Classify this cell by malaria status.
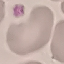
Uninfected.

Thin smear of blood. Giemsa-stained preparation. Acquired by smartphone through the microscope eyepiece. Automatically extracted cell patch, resized to 64 × 64 pixels.